State which cell type is depicted.
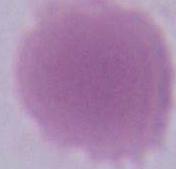

An erythrocyte.

magnification: 1000x
modality: micrograph